Outline each blood parasite and name the species.
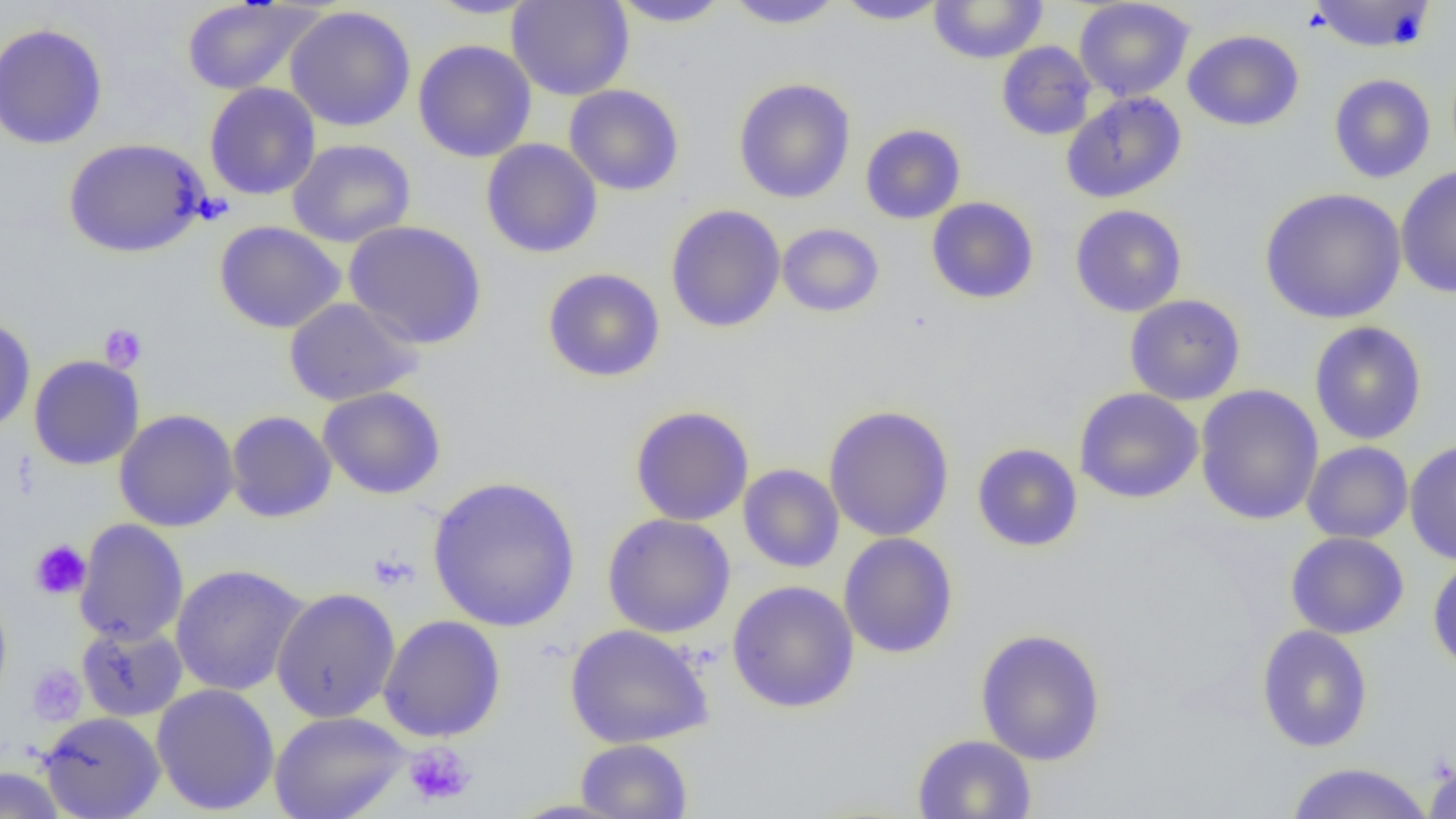
No blood parasites observed.

Approximate bounding boxes as (x1,y1)-(x2,y2) corner pairs in pixels. Platelet locations: (99,323)-(147,372), (30,540)-(91,600), (367,551)-(418,592), (26,663)-(87,725), (404,741)-(476,807). Uninfected red blood cell locations: (424,0)-(543,20), (506,0)-(634,101), (724,0)-(845,30), (834,0)-(950,25), (1073,0)-(1195,101), (1308,0)-(1436,53), (180,1)-(322,96), (611,1)-(732,27), (928,1)-(1049,64), (285,6)-(416,132), (0,23)-(108,150), (1183,30)-(1304,131), (412,39)-(537,163), (996,41)-(1096,141), (1328,74)-(1436,183), (733,78)-(856,204), (204,83)-(321,200), (564,84)-(685,196), (1061,91)-(1187,203), (860,124)-(966,224), (63,137)-(209,258), (287,139)-(416,248), (481,139)-(603,258), (1395,165)-(1456,298), (1259,187)-(1407,324), (926,197)-(1039,304), (665,204)-(786,332), (1069,204)-(1187,317), (215,220)-(345,334), (343,220)-(487,349), (776,223)-(885,318), (542,268)-(665,382), (1124,294)-(1246,406), (284,297)-(423,407), (0,316)-(36,435), (1309,321)-(1427,446), (1105,325)-(1236,446), (29,355)-(145,470), (1194,384)-(1324,526), (318,386)-(446,500), (1074,388)-(1203,504), (824,404)-(955,542), (629,405)-(754,526), (114,409)-(239,532), (225,410)-(337,522), (1404,439)-(1456,565), (1301,441)-(1413,544), (971,442)-(1083,552), (738,464)-(844,573), (427,475)-(581,633), (602,513)-(736,638), (74,518)-(189,647), (1285,531)-(1409,639), (839,532)-(958,659), (1427,553)-(1456,676), (170,563)-(309,697), (726,580)-(859,714), (0,587)-(13,709), (270,587)-(401,723), (378,614)-(506,742), (76,623)-(188,722), (563,623)-(714,749), (1256,625)-(1373,753), (975,628)-(1106,766), (151,683)-(280,816), (269,710)-(411,819), (38,711)-(165,819), (912,734)-(1036,819), (575,738)-(692,819), (1423,758)-(1456,819), (1283,762)-(1435,819), (0,765)-(66,819), (505,797)-(635,818). Slide-level diagnosis: no evidence of blood parasites. Single field of view. Light microscopy. Thin blood film. Image is 1456×819 pixels. Captured at 1000x magnification.